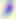
magnification = 400x
modality = micrograph
identification = Toxoplasma gondii